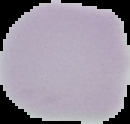
Summary:
  - Image size: 130×124 pixels
  - Image type: cell region segmented out of the field of view; surrounding area masked to black
  - Malaria status: uninfected
  - Preparation: thin blood smear